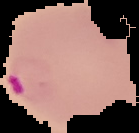

From a thin blood smear. The area outside the segmented cell region is set to black. Image is 139×133 pixels. Result: Plasmodium parasites detected.